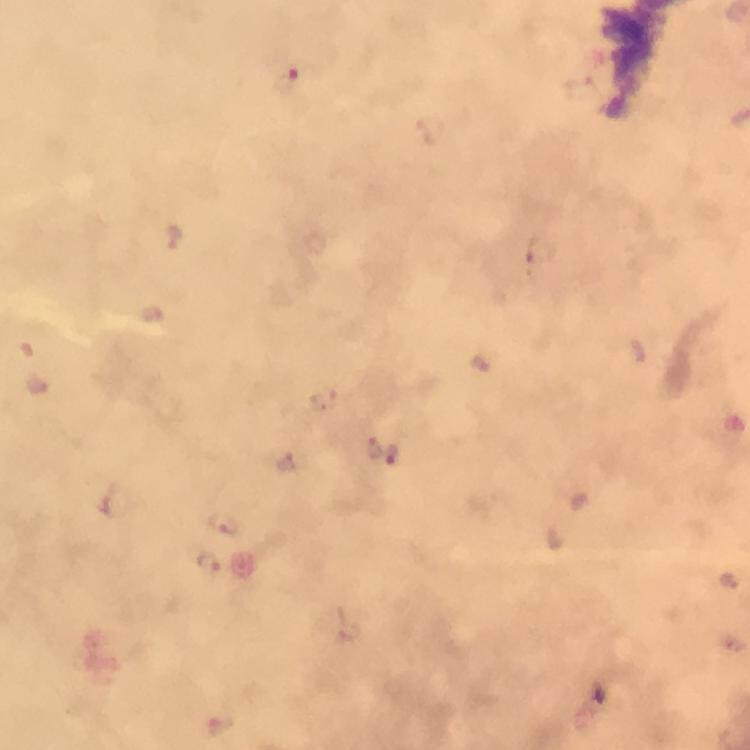

Approximate centers as (x, y) in pixels.
Summary:
  - Plasmodium parasite locations: (285, 82), (173, 237), (541, 253), (480, 362), (372, 447), (393, 454), (287, 462), (224, 524), (209, 565), (221, 727)
  - Magnification: 100x
  - Cropped from: a single field of view
  - Preparation: thick blood film
  - Stain: Giemsa
  - Context: from a malaria diagnostic workup
  - Capture: smartphone mounted on the microscope
  - Image size: 750×750 pixels
  - Immersion oil: used